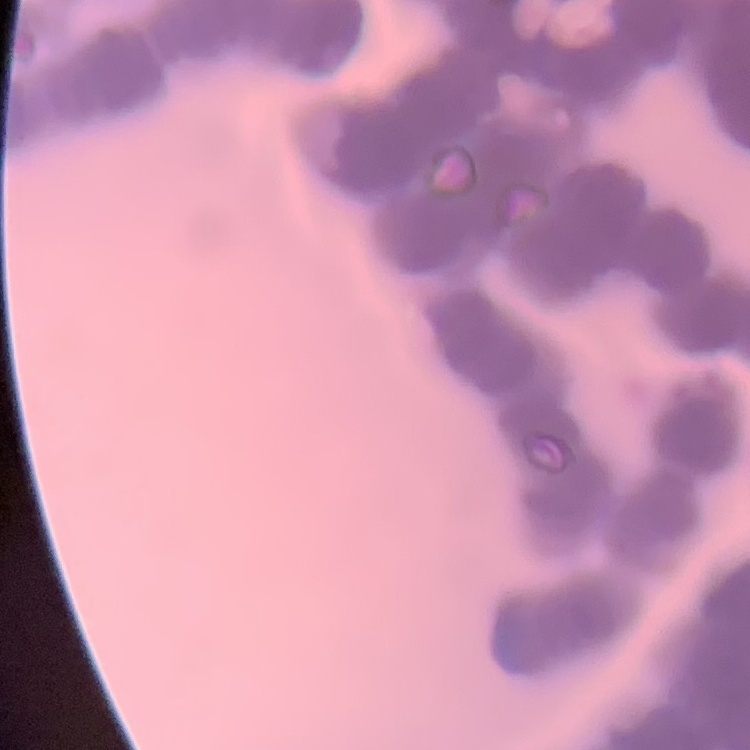

erythrocyte morphology = rouleaux formation
image type = square crop of a larger photomicrograph
preparation = thin peripheral smear
stain = Field's or Giemsa